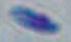
Summary:
  - Modality: photomicrograph
  - Magnification: 1000x
  - Identification: Toxoplasma gondii